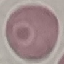
result: negative for malaria parasites
capture: smartphone through the microscope eyepiece
image_type: automatically extracted cell patch, resized to 64 × 64 pixels
preparation: thin blood film
stain: Giemsa